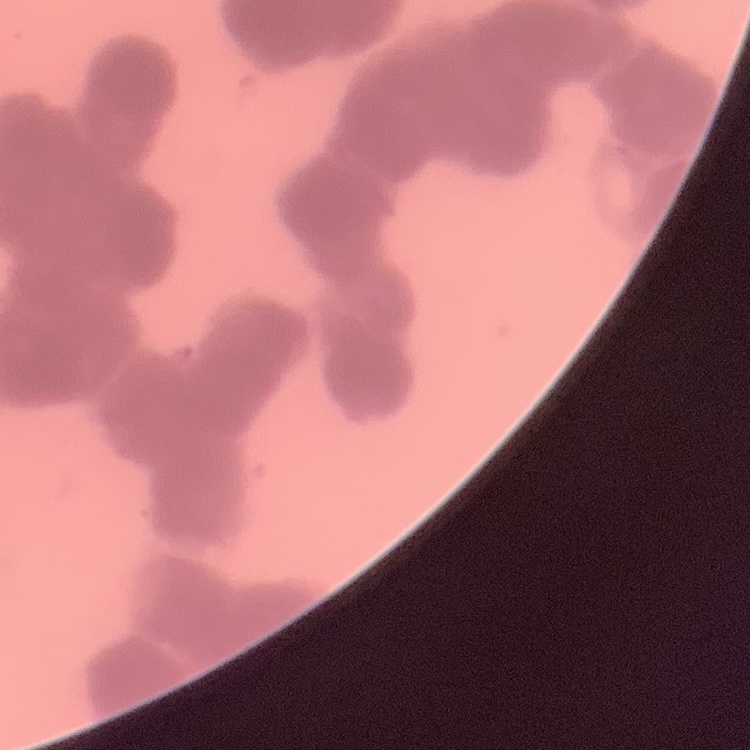

The red blood cells exhibit rouleaux formation. Thin blood film. Stained with either Field's or Giemsa. One tile cut from a larger photomicrograph.